State which parasite is depicted.
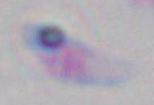

This is Toxoplasma gondii.

Micrograph. Captured at 1000x magnification.